Locate every malaria parasite.
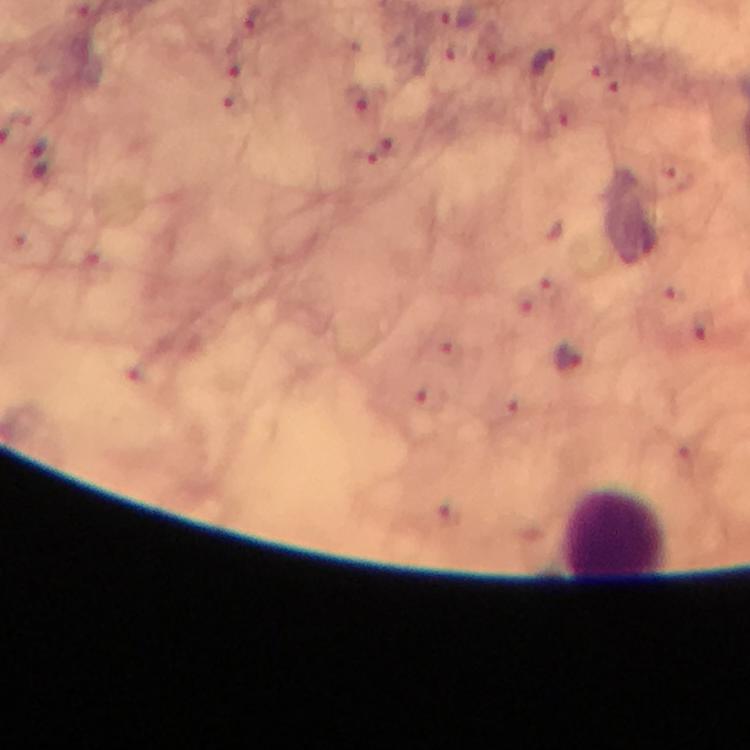
Approximate centers as [x, y] in pixels.
Malaria parasites: [450, 23], [542, 62], [238, 63], [358, 97], [40, 160], [567, 356].

Summary:
  - Leukocyte locations: [615, 536]
  - Preparation: thick smear
  - Context: from a diagnostic examination for malaria
  - Magnification: 100x
  - Cropped from: a single field of view
  - Immersion oil: used
  - Capture: smartphone mounted on the microscope
  - Stain: Giemsa
  - Image size: 750×750 pixels